Classify this cell by malaria status.
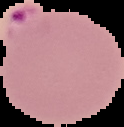
It is parasitized.

image type = cell region segmented out of the field of view; surrounding area masked to black
image size = 124×127 pixels
preparation = thin blood smear